Classify this cell by malaria status.
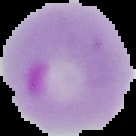
It is parasitized.

Summary:
  - Image size: 136×136 pixels
  - Image type: segmented cell region with the area outside set to black
  - Preparation: thin blood smear